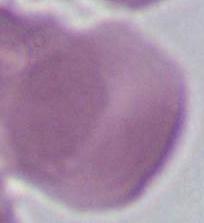
identification: red blood cell
modality: micrograph
magnification: 1000x